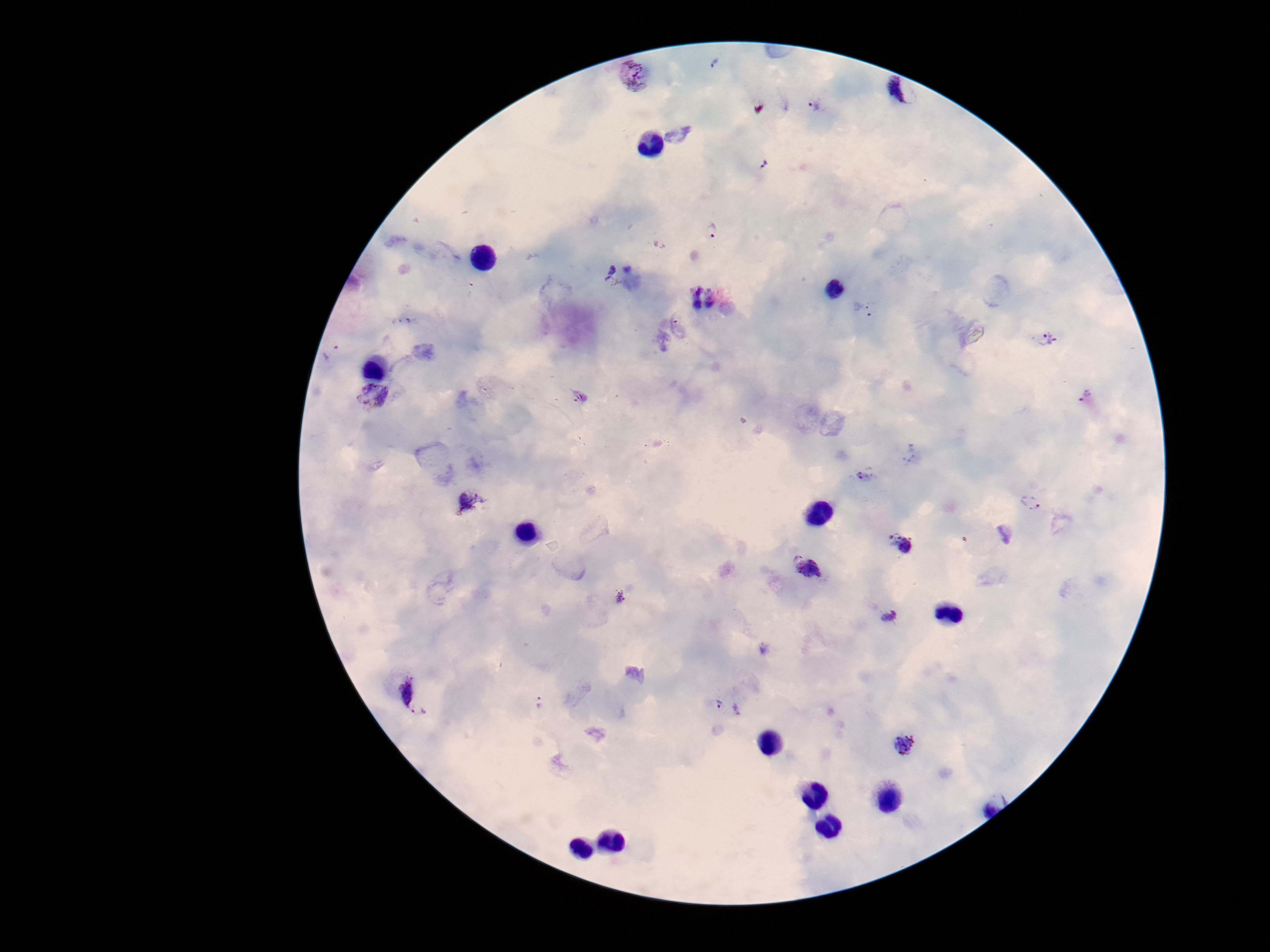
patient malaria status = positive
stain = Giemsa
magnification = 100x
image size = 1270×952 pixels
preparation = thick blood smear
Plasmodium parasite locations = approximate centers as (x, y) in pixels: (715, 64), (635, 76), (895, 96), (814, 105), (765, 166), (712, 230), (613, 276), (702, 297), (872, 309), (1049, 340), (330, 353), (374, 396), (1086, 396), (868, 475), (468, 500), (1030, 502), (901, 542), (805, 565), (620, 597), (888, 616), (412, 698), (539, 702), (718, 704), (737, 709), (904, 745)
capture = smartphone camera through the microscope eyepiece
field of view = single